Assess this cell for malaria.
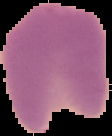
Parasitized.

preparation = thin blood smear
image type = segmented cell region on a black background
image size = 112×136 pixels